Assess this cell for malaria.
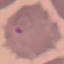

It is parasitized.

Summary:
  - Stain: Giemsa
  - Image type: automatically extracted cell patch, resized to 64 × 64 pixels
  - Preparation: thin blood film
  - Capture: smartphone camera at the microscope eyepiece